Comment on the morphology of the erythrocytes.
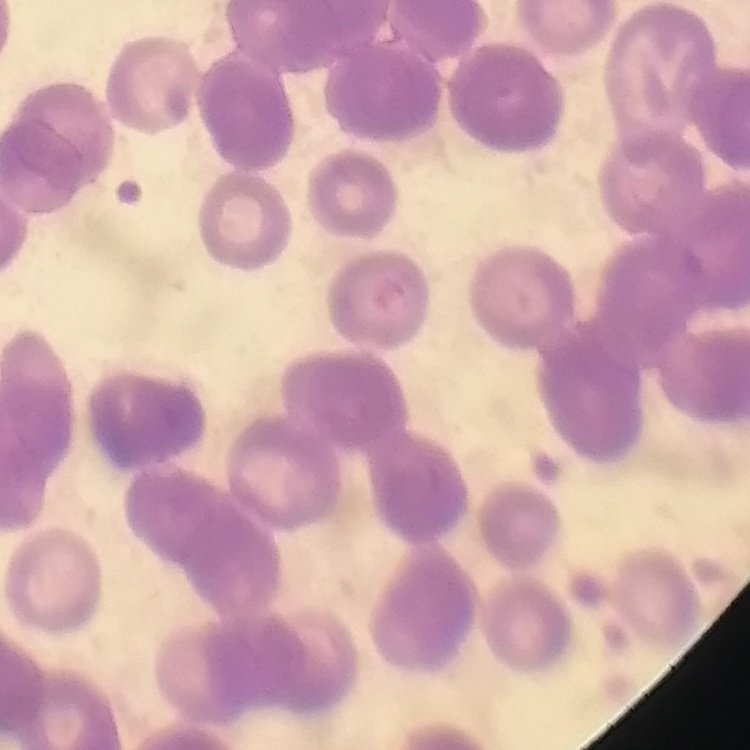
Rouleaux formation.

Summary:
  - Preparation: thin peripheral smear
  - Stain: Field's or Giemsa
  - Image type: one tile cut from a larger photomicrograph